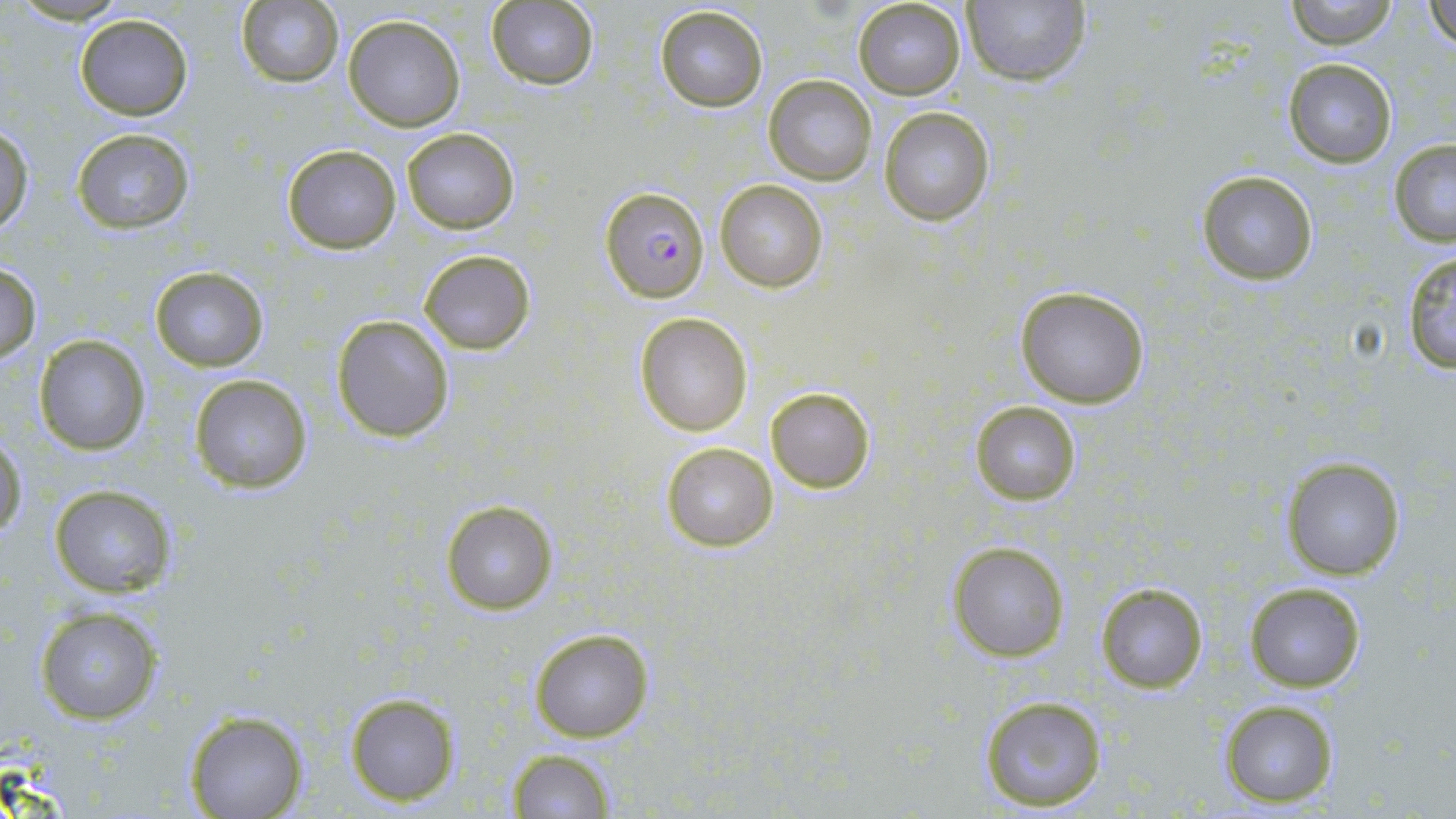 Approximate bounding boxes as (x1, y1, x2, y2) in pixels. Uninfected red blood cell locations: (234, 0, 346, 87), (853, 0, 966, 99), (1286, 0, 1398, 49), (961, 1, 1091, 86), (1427, 1, 1455, 53), (486, 2, 598, 90), (655, 5, 768, 113), (74, 14, 192, 120), (344, 16, 465, 131), (1283, 59, 1395, 167), (763, 74, 877, 186), (879, 107, 995, 225), (0, 124, 35, 236), (401, 128, 520, 235), (70, 129, 196, 233), (1389, 139, 1456, 246), (281, 143, 401, 255), (1196, 170, 1320, 284), (713, 177, 830, 293), (419, 249, 536, 355), (1399, 251, 1456, 376), (0, 262, 43, 365), (149, 265, 270, 370), (1014, 283, 1151, 408), (635, 311, 753, 436), (331, 313, 455, 443), (34, 336, 152, 456), (189, 373, 314, 494), (765, 386, 876, 495), (969, 400, 1082, 506), (0, 433, 27, 539), (660, 440, 777, 551), (1280, 454, 1407, 580), (49, 484, 177, 598), (441, 500, 559, 616), (948, 542, 1069, 662), (1244, 579, 1367, 693), (1095, 580, 1209, 695), (35, 607, 163, 724), (529, 627, 653, 744), (345, 692, 459, 805), (976, 693, 1109, 811), (1217, 699, 1340, 808), (183, 709, 309, 819), (506, 749, 616, 818). Plasmodium falciparum-infected red blood cell locations: (600, 185, 709, 302). Slide-level diagnosis: Plasmodium falciparum. Single field of view. May-Grünwald-Giemsa stain. 1000x magnification. Thin blood smear. Optical microscopy. Image is 1456×819 pixels.